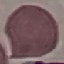
Summary:
  - Result: no malaria parasites seen
  - Image type: cell patch, automatically extracted from a larger field of view and resized to 64 × 64 pixels
  - Preparation: thin blood film
  - Stain: Giemsa
  - Capture: smartphone camera at the microscope eyepiece